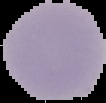
{
  "result": "no malaria parasites detected",
  "image_type": "cell region segmented out of the field of view; surrounding area masked to black",
  "image_size": "106×103 pixels",
  "preparation": "thin blood smear"
}